State which cell type is depicted.
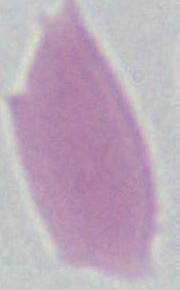

This is an erythrocyte.

Summary:
  - Modality: photomicrograph
  - Magnification: 1000x